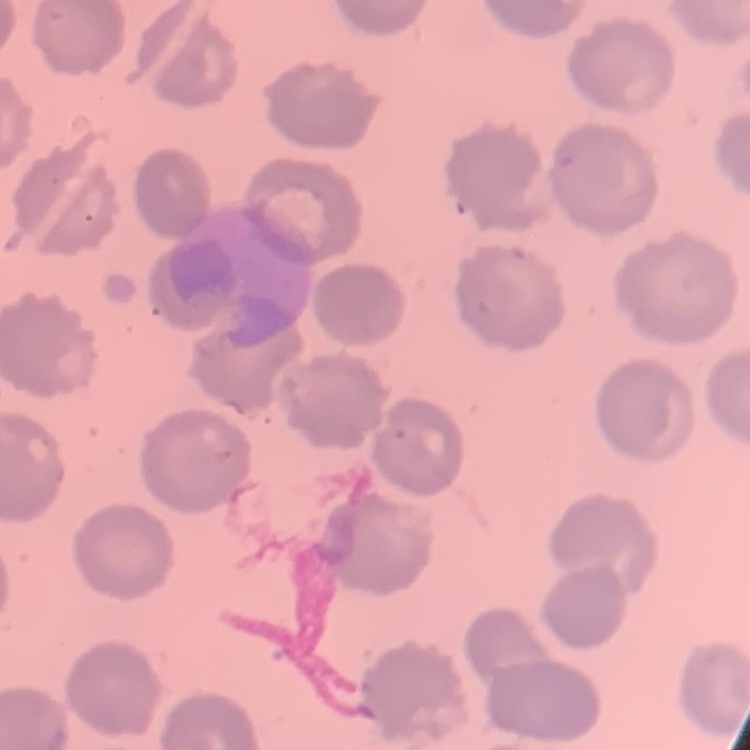

Summary:
  - Red blood cell morphology: no rouleaux formation
  - Preparation: thin peripheral smear
  - Image type: square crop of a larger photomicrograph
  - Stain: Field's or Giemsa